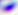

Summary:
  - Modality: micrograph
  - Magnification: 400x
  - Identification: Toxoplasma gondii